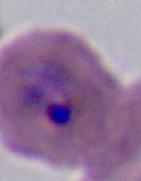
A Plasmodium parasite is seen. Micrograph. 400x or 1000x magnification.